Locate every malaria parasite and every leukocyte.
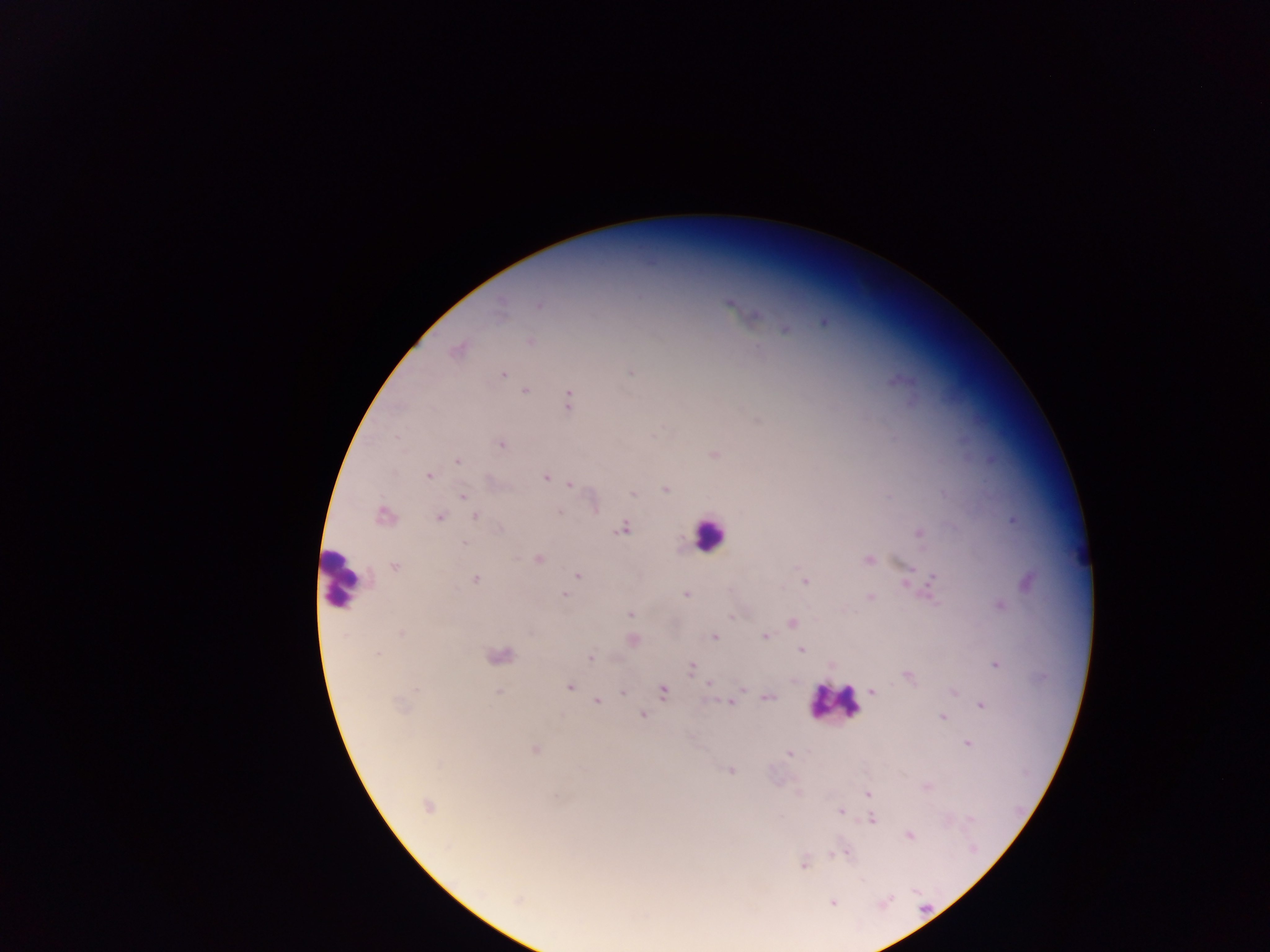

Approximate centers as {x, y} in pixels.
Malaria parasites: {730, 303}, {539, 304}, {754, 315}, {824, 321}, {785, 329}, {529, 341}, {458, 349}, {631, 372}, {502, 375}, {898, 379}, {525, 390}, {568, 400}, {501, 444}, {713, 453}, {457, 460}, {428, 475}, {546, 477}, {570, 484}, {665, 488}, {631, 493}, {462, 495}, {559, 512}, {384, 515}, {475, 516}, {438, 517}, {1012, 519}, {622, 528}, {918, 533}, {463, 543}, {538, 559}, {868, 559}, {394, 566}, {907, 571}, {577, 574}, {476, 579}, {907, 580}, {933, 580}, {804, 581}, {1027, 581}, {564, 594}, {686, 594}, {870, 596}, {998, 606}, {630, 614}, {791, 623}, {401, 633}, {765, 636}, {714, 637}, {631, 639}, {800, 649}, {376, 655}, {498, 655}, {591, 658}, {996, 664}, {692, 667}, {908, 675}, {709, 683}, {569, 686}, {498, 691}, {662, 691}, {871, 691}, {953, 691}, {622, 693}, {766, 696}, {597, 701}, {730, 702}, {981, 705}, {642, 714}, {942, 717}, {967, 742}, {534, 748}, {790, 753}, {731, 770}, {926, 786}, {868, 795}, {427, 804}, {840, 811}, {871, 818}, {909, 835}, {843, 851}, {804, 865}, {517, 899}, {832, 902}.
Leukocytes: {709, 534}, {341, 578}, {834, 702}.

country = Ghana
capture = mobile-phone photograph through a microscope
field of view = single
image size = 1270×952 pixels
preparation = thick blood film